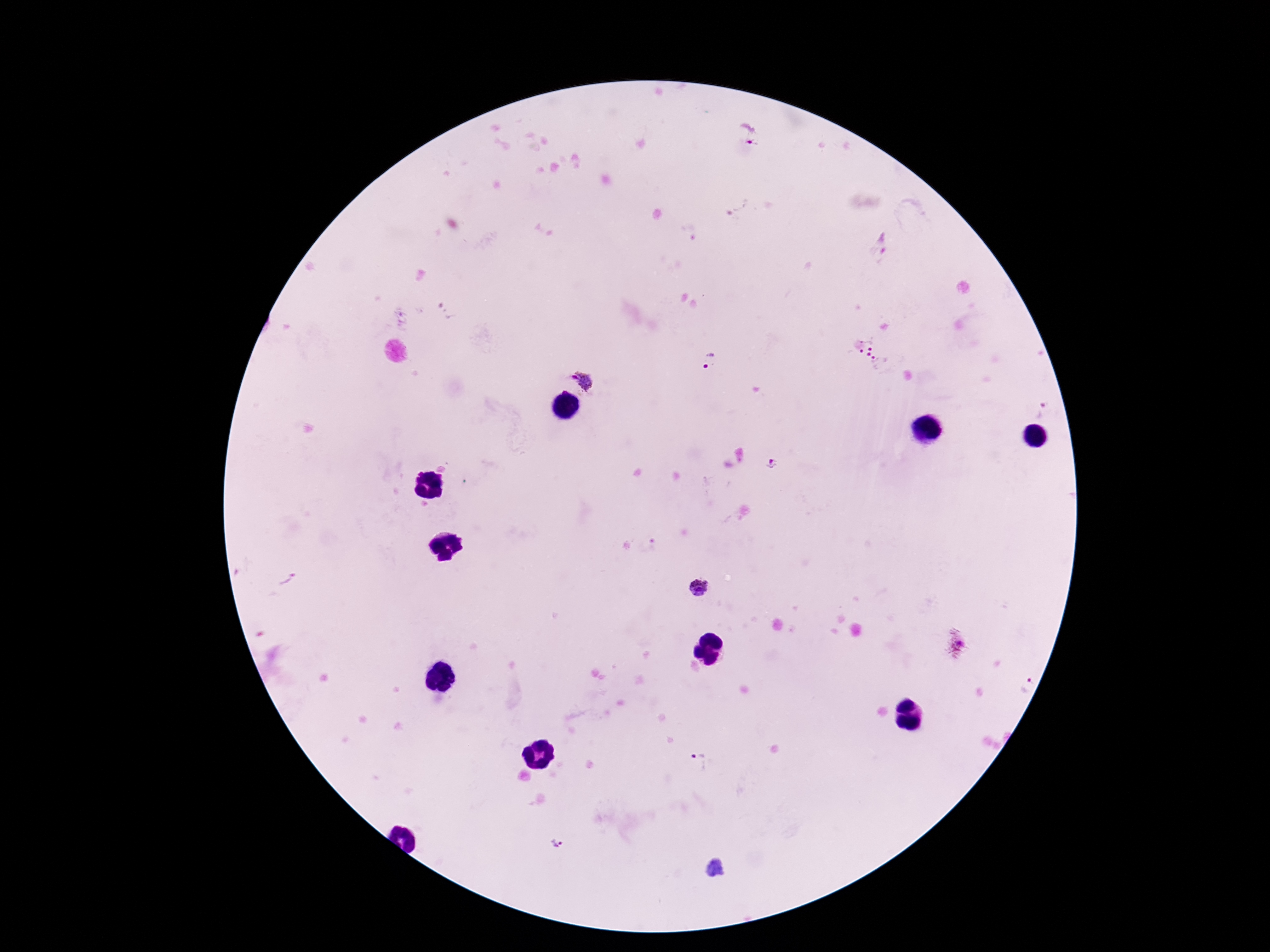

Approximate centers as (x, y) in pixels. Plasmodium parasite locations: (750, 134), (737, 207), (882, 245), (875, 353), (708, 360), (584, 379), (1041, 409), (772, 463), (698, 588), (957, 644), (701, 763), (556, 843). Giemsa stain. One field from this slide. Thick peripheral-blood smear. 100x magnification. Image is 1270×952 pixels. Smartphone photograph taken through the microscope eyepiece. Patient malaria status: positive.